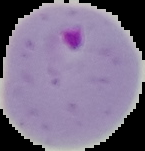
Summary:
  - Image type: segmented cell region on a black background
  - Result: malaria parasites detected
  - Preparation: thin blood smear
  - Image size: 145×151 pixels